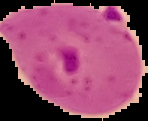

Result: malaria parasites identified. Cell region segmented out of the field of view; the surrounding area is masked to black. Image is 148×121 pixels. From a thin blood smear.